Give the preparation type.
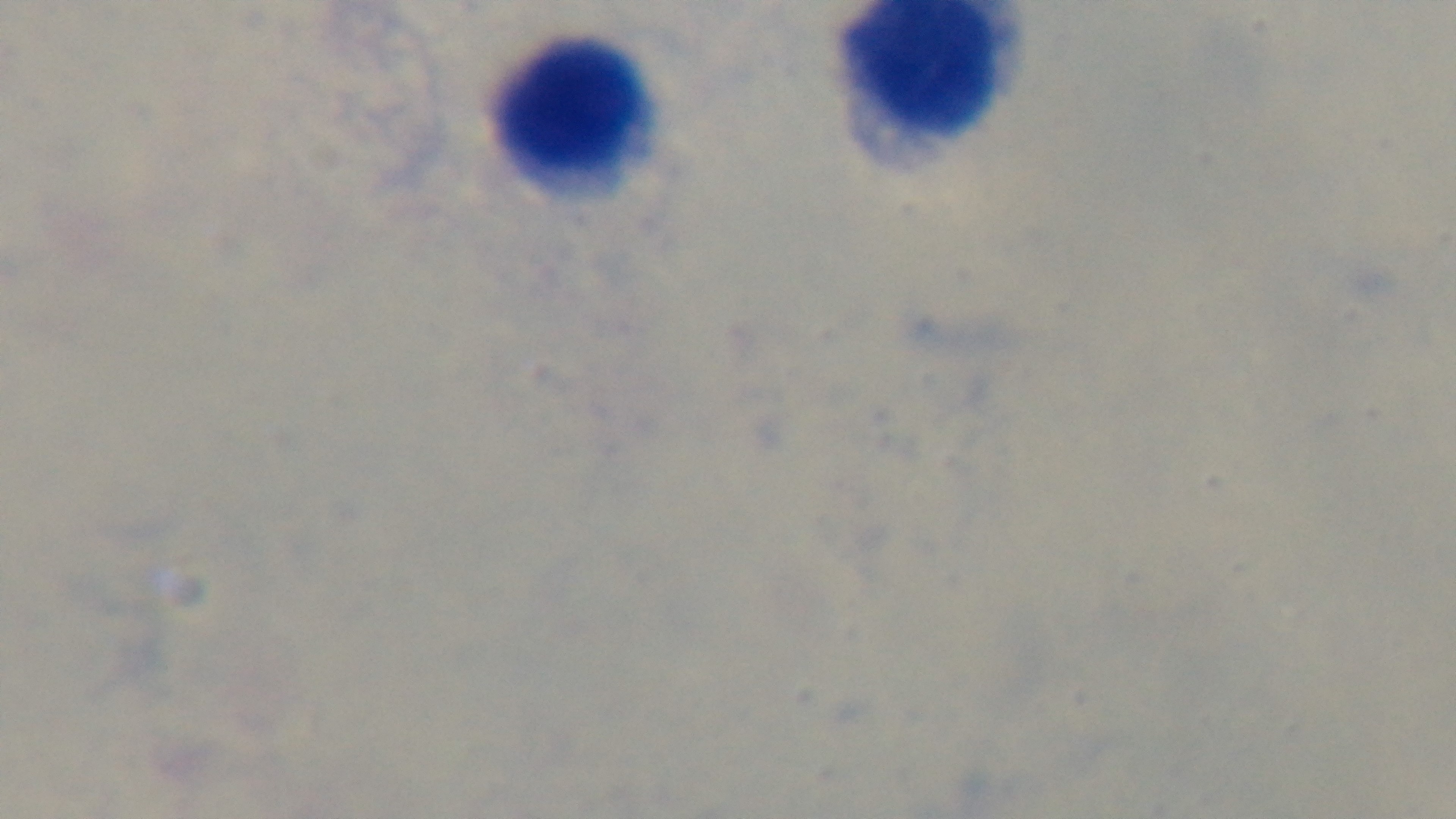
A thick smear.

Single field of view. Malaria status: uninfected. Photomicrograph. Mounted 4K digital camera. Giemsa-stained. 100x oil-immersion objective.